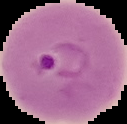

Summary:
  - Malaria status: parasitized
  - Image type: segmented cell region on a black background
  - Preparation: thin blood film
  - Image size: 127×124 pixels